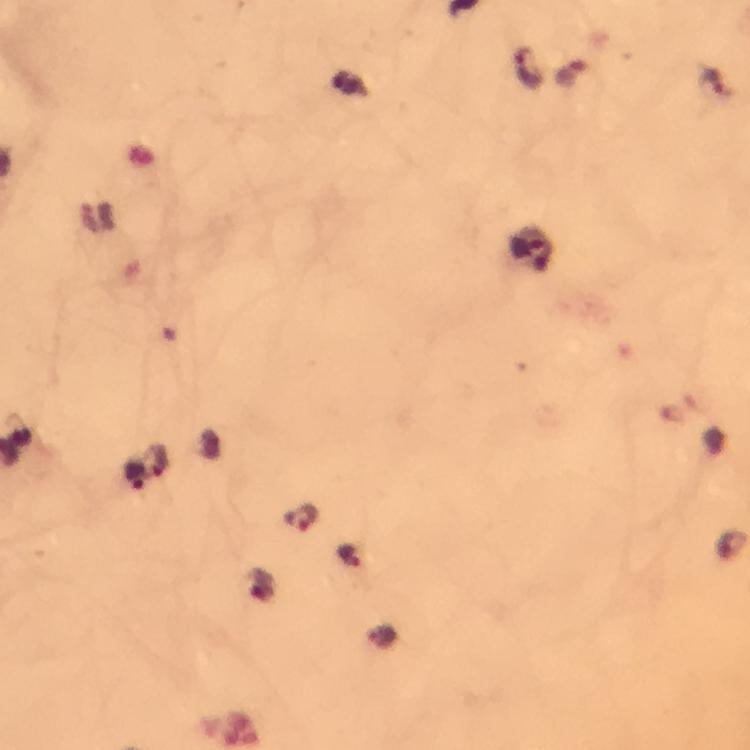
Approximate centers as [x, y] in pixels.
Summary:
  - Plasmodium parasite locations: [527, 67], [712, 83], [526, 246], [134, 477], [304, 518], [349, 555]
  - Preparation: thick smear
  - Stain: Giemsa
  - Cropped from: one field of view
  - Magnification: 100x
  - Capture: smartphone camera through the microscope
  - Context: from a diagnostic examination for malaria
  - Immersion oil: applied
  - Image size: 750×750 pixels